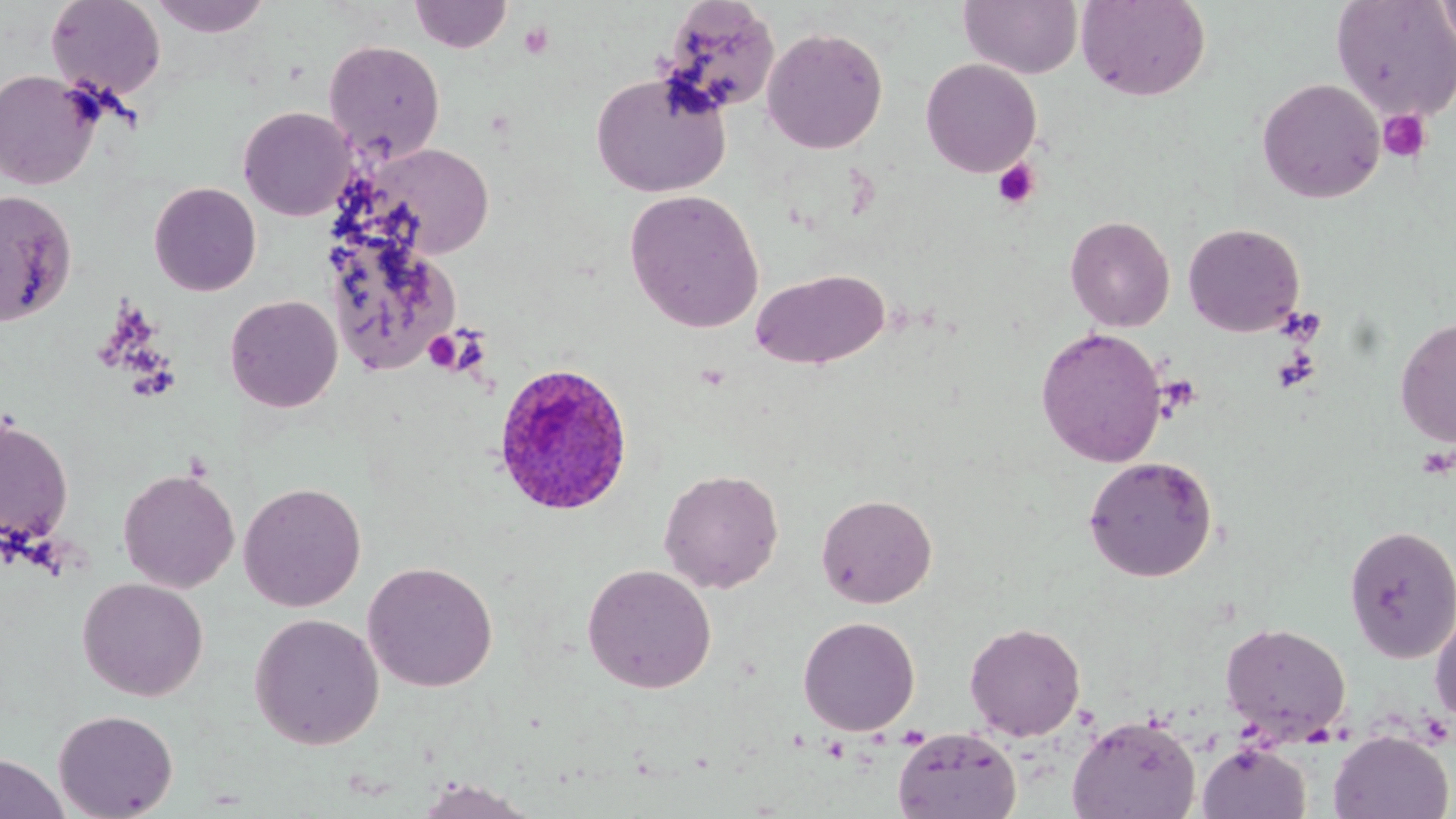
Summary:
  - Coordinate format: approximate bounding boxes as named x1/y1/x2/y2 corners in pixels
  - Uninfected red blood cell locations: (x1=46, y1=0, x2=167, y2=102), (x1=148, y1=0, x2=273, y2=38), (x1=410, y1=0, x2=513, y2=53), (x1=959, y1=0, x2=1084, y2=79), (x1=1076, y1=0, x2=1211, y2=101), (x1=1331, y1=0, x2=1456, y2=121), (x1=1436, y1=0, x2=1456, y2=56), (x1=657, y1=2, x2=781, y2=117), (x1=762, y1=26, x2=888, y2=154), (x1=323, y1=39, x2=446, y2=163), (x1=921, y1=58, x2=1041, y2=177), (x1=0, y1=69, x2=101, y2=190), (x1=590, y1=70, x2=731, y2=198), (x1=1257, y1=78, x2=1386, y2=204), (x1=238, y1=106, x2=357, y2=221), (x1=365, y1=142, x2=493, y2=258), (x1=149, y1=182, x2=262, y2=296), (x1=624, y1=189, x2=764, y2=333), (x1=0, y1=190, x2=78, y2=326), (x1=1065, y1=215, x2=1175, y2=332), (x1=1182, y1=222, x2=1305, y2=337), (x1=321, y1=223, x2=461, y2=376), (x1=750, y1=268, x2=890, y2=370), (x1=225, y1=295, x2=343, y2=412), (x1=1395, y1=317, x2=1456, y2=449), (x1=1035, y1=326, x2=1168, y2=468), (x1=0, y1=415, x2=74, y2=547), (x1=1082, y1=455, x2=1218, y2=582), (x1=118, y1=467, x2=240, y2=593), (x1=658, y1=468, x2=784, y2=593), (x1=238, y1=481, x2=366, y2=612), (x1=816, y1=492, x2=938, y2=608), (x1=1343, y1=524, x2=1456, y2=663), (x1=362, y1=561, x2=499, y2=692), (x1=581, y1=563, x2=717, y2=693), (x1=77, y1=577, x2=209, y2=701), (x1=1429, y1=605, x2=1456, y2=726), (x1=249, y1=612, x2=384, y2=750), (x1=798, y1=616, x2=920, y2=736), (x1=964, y1=622, x2=1086, y2=740), (x1=1220, y1=622, x2=1351, y2=744), (x1=53, y1=708, x2=178, y2=819), (x1=1066, y1=713, x2=1201, y2=819), (x1=891, y1=727, x2=1022, y2=819), (x1=1328, y1=729, x2=1454, y2=818), (x1=1197, y1=741, x2=1312, y2=819), (x1=0, y1=753, x2=69, y2=819), (x1=411, y1=778, x2=541, y2=819)
  - Plasmodium ovale-infected red blood cell locations: (x1=492, y1=361, x2=634, y2=516)
  - Platelet locations: (x1=518, y1=22, x2=554, y2=59), (x1=1377, y1=109, x2=1432, y2=163), (x1=993, y1=158, x2=1040, y2=209), (x1=424, y1=331, x2=463, y2=372)
  - Slide-level diagnosis: Plasmodium ovale
  - Image size: 1456×819 pixels
  - Stain: May-Grünwald-Giemsa
  - Preparation: thin blood smear
  - Field of view: one of a larger specimen
  - Magnification: 1000x
  - Modality: optical microscopy